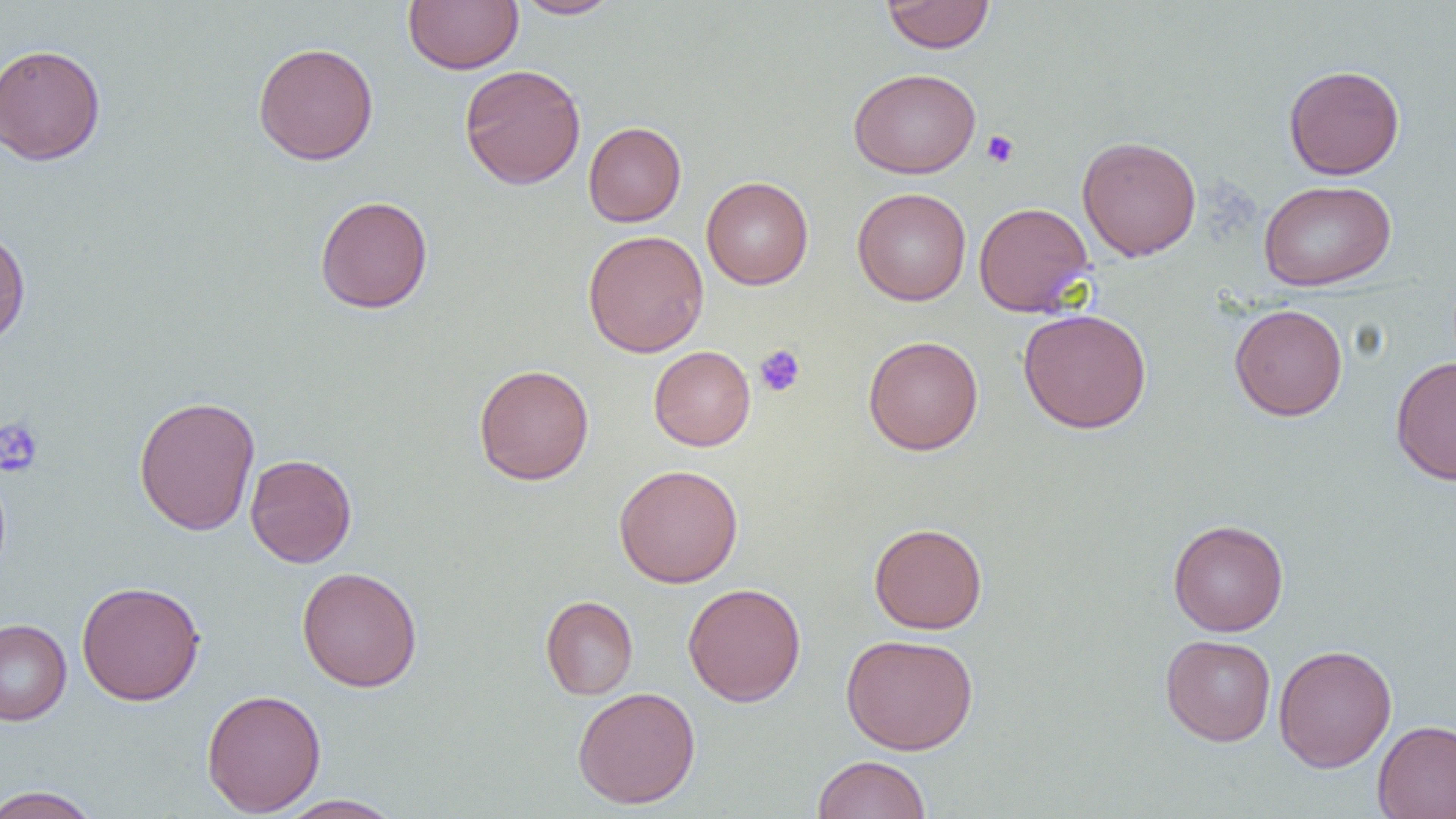

Summary:
  - Coordinate format: approximate bounding boxes as [x1, y1, x2, y2] in pixels
  - Uninfected red blood cell locations: [403, 0, 523, 74], [513, 0, 623, 19], [881, 0, 995, 54], [253, 41, 379, 165], [0, 43, 105, 166], [458, 64, 586, 190], [1283, 64, 1405, 180], [848, 68, 981, 179], [583, 121, 687, 226], [1076, 135, 1202, 261], [701, 176, 813, 289], [1258, 179, 1396, 291], [852, 187, 971, 305], [315, 195, 433, 314], [973, 202, 1094, 317], [0, 226, 31, 348], [583, 229, 709, 358], [1229, 304, 1348, 421], [1018, 308, 1152, 434], [863, 335, 984, 455], [648, 345, 756, 451], [1390, 356, 1456, 484], [473, 364, 595, 486], [133, 395, 261, 536], [244, 454, 357, 568], [613, 464, 744, 588], [1167, 519, 1289, 636], [868, 522, 987, 634], [296, 566, 423, 692], [76, 581, 205, 706], [683, 582, 806, 707], [540, 595, 639, 700], [0, 619, 72, 726], [840, 633, 978, 755], [1160, 634, 1276, 746], [1273, 644, 1397, 772], [572, 686, 701, 809], [201, 688, 326, 817], [1372, 719, 1456, 818], [813, 754, 931, 819], [0, 785, 103, 819], [273, 794, 406, 818]
  - Platelet locations: [981, 130, 1019, 168], [754, 344, 806, 397], [0, 418, 43, 476]
  - Slide-level diagnosis: no evidence of blood parasites
  - Modality: optical microscopy
  - Preparation: thin blood smear
  - Magnification: 1000x
  - Field of view: single
  - Image size: 1456×819 pixels